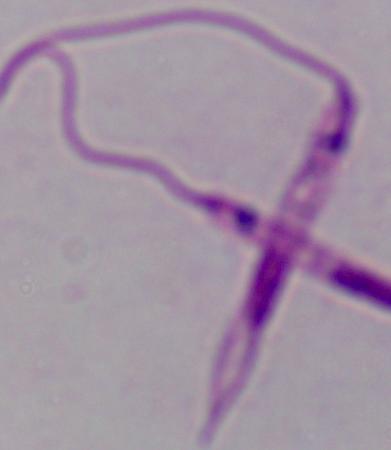
Captured at 1000x magnification. A Leishmania parasite is seen. Micrograph.